State which cell type is depicted.
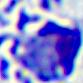
This is a leukocyte.

Summary:
  - Modality: micrograph
  - Magnification: 400x